Comment on the morphology of the erythrocytes.
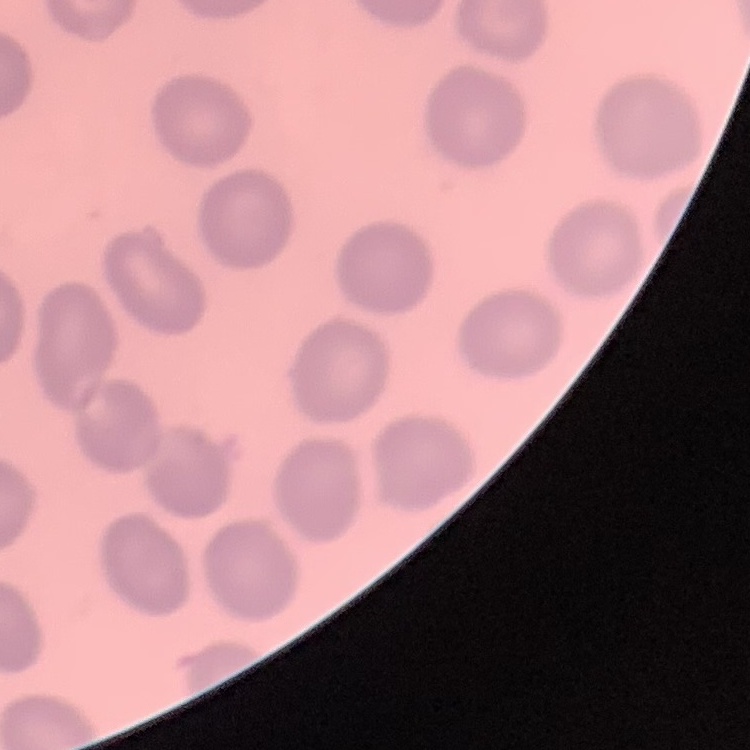
They show no rouleaux formation.

Square crop of a larger photomicrograph. Thin peripheral smear. Stained with either Field's or Giemsa.